Identify the parasite.
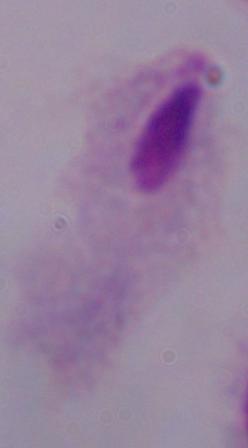
This is a trichomonad.

Summary:
  - Modality: micrograph
  - Magnification: 1000x